Name the blood parasite species.
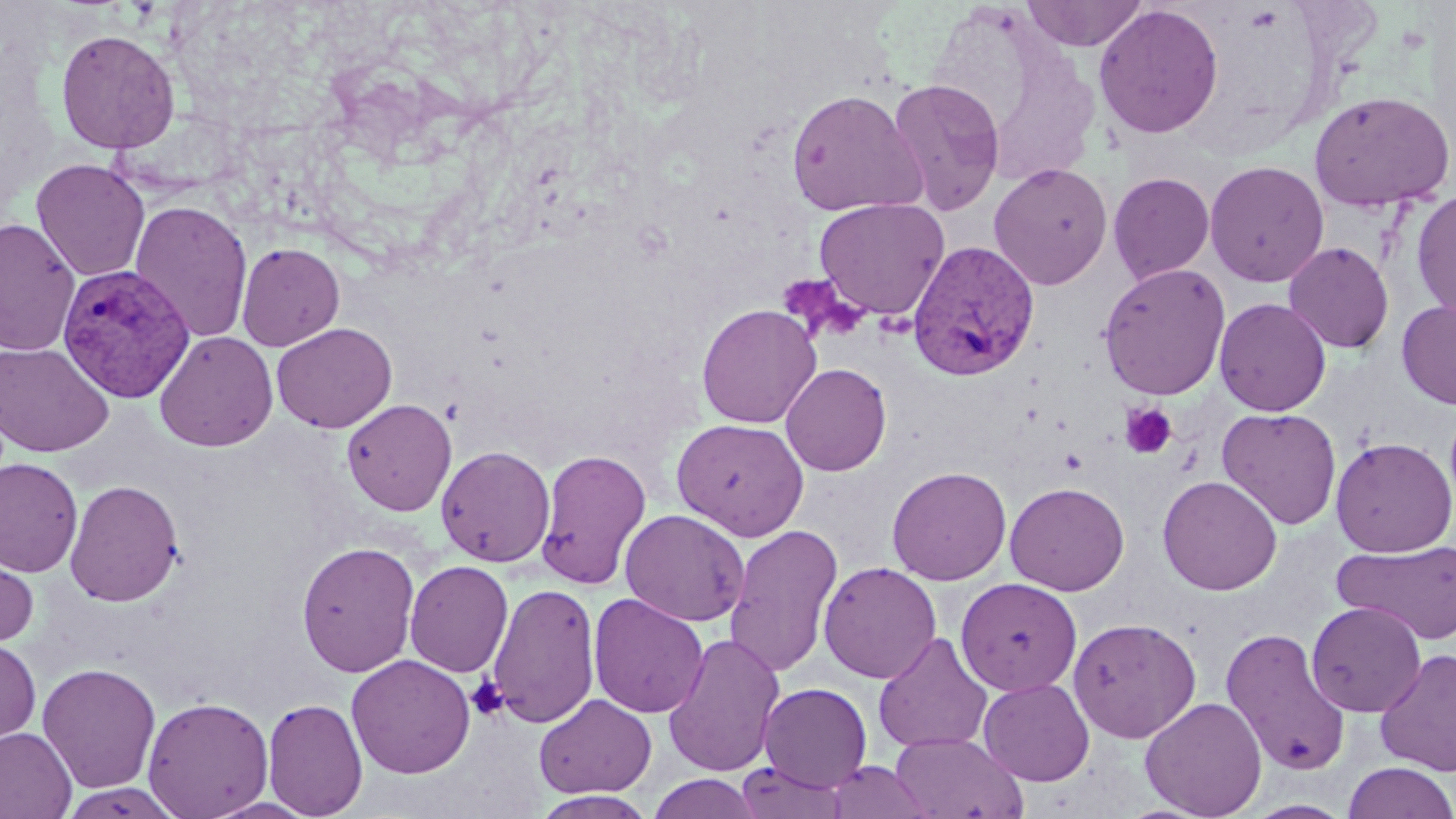
Plasmodium vivax.

image size = 1456×819 pixels
modality = light microscopy
platelet locations = approximate bounding boxes as [x1, y1, x2, y2] in pixels: [1120, 402, 1178, 459], [468, 676, 509, 721]
field of view = single
magnification = 1000x
stain = May-Grünwald-Giemsa
Plasmodium vivax-infected red blood cell locations = approximate bounding boxes as [x1, y1, x2, y2] in pixels: [906, 241, 1040, 381], [57, 264, 195, 402]
uninfected red blood cell locations = approximate bounding boxes as [x1, y1, x2, y2] in pixels: [1021, 0, 1149, 51], [924, 4, 1103, 187], [1093, 4, 1224, 138], [55, 28, 180, 154], [887, 78, 1007, 216], [785, 88, 927, 217], [1308, 90, 1455, 212], [31, 158, 150, 282], [1205, 160, 1329, 286], [988, 162, 1113, 290], [1108, 172, 1215, 284], [1411, 187, 1456, 324], [814, 197, 949, 320], [129, 200, 253, 343], [0, 218, 81, 357], [1283, 241, 1395, 353], [236, 242, 345, 351], [1098, 263, 1232, 400], [1213, 297, 1331, 416], [1396, 299, 1456, 410], [696, 303, 821, 428], [271, 322, 397, 433], [154, 331, 277, 451], [0, 341, 114, 457], [780, 362, 892, 476], [341, 398, 457, 516], [1217, 407, 1342, 529], [671, 418, 810, 539], [1330, 436, 1455, 556], [436, 445, 556, 567], [535, 448, 652, 590], [0, 457, 82, 578], [886, 465, 1012, 585], [1157, 475, 1283, 595], [65, 479, 184, 606], [1004, 481, 1129, 595], [620, 508, 750, 626], [724, 523, 843, 679], [296, 540, 420, 677], [1333, 540, 1456, 645], [0, 541, 39, 653], [404, 560, 513, 677], [818, 561, 942, 684], [955, 577, 1082, 696], [486, 581, 602, 729], [588, 593, 709, 718], [1306, 601, 1426, 717], [1068, 617, 1202, 743], [1220, 627, 1351, 776], [662, 631, 785, 777], [873, 632, 994, 753], [0, 638, 41, 749], [1374, 648, 1456, 776], [346, 654, 476, 779], [37, 662, 161, 794], [978, 677, 1095, 786], [759, 682, 873, 791], [533, 693, 657, 799], [142, 696, 274, 818], [1140, 696, 1267, 818], [262, 697, 368, 819], [0, 727, 76, 818], [890, 732, 1028, 818], [733, 761, 850, 819], [825, 761, 937, 819], [1341, 761, 1456, 819], [646, 773, 764, 818], [531, 791, 659, 818]
preparation = thin blood film